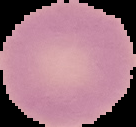
Malaria status: uninfected. Segmented cell region on a black background. Image is 136×127 pixels. From a thin blood smear.